Comment on the morphology of the red blood cells.
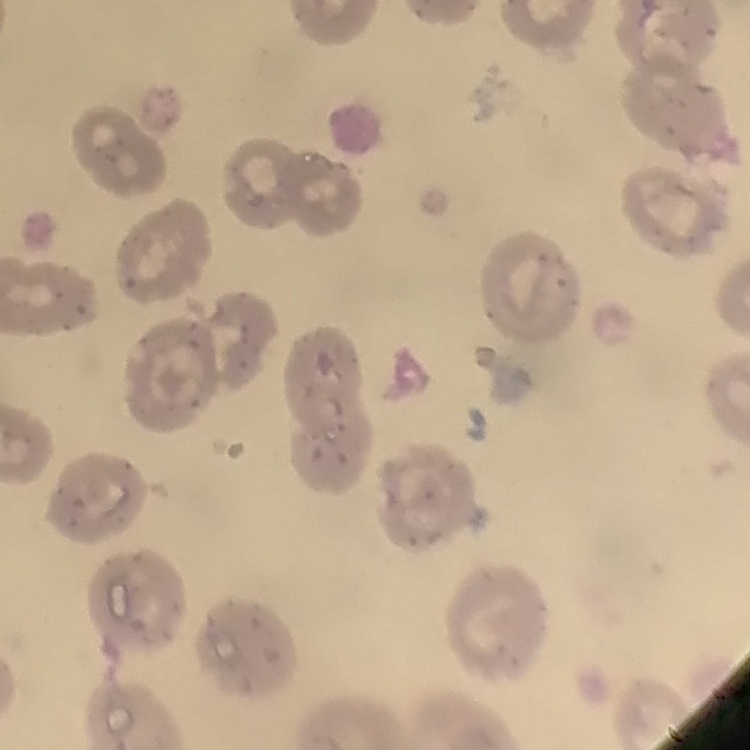

No rouleaux formation.

Summary:
  - Preparation: thin peripheral smear
  - Stain: Field's or Giemsa
  - Image type: square crop of a larger photomicrograph